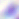

{
  "identification": "Toxoplasma gondii",
  "modality": "photomicrograph",
  "magnification": "400x"
}